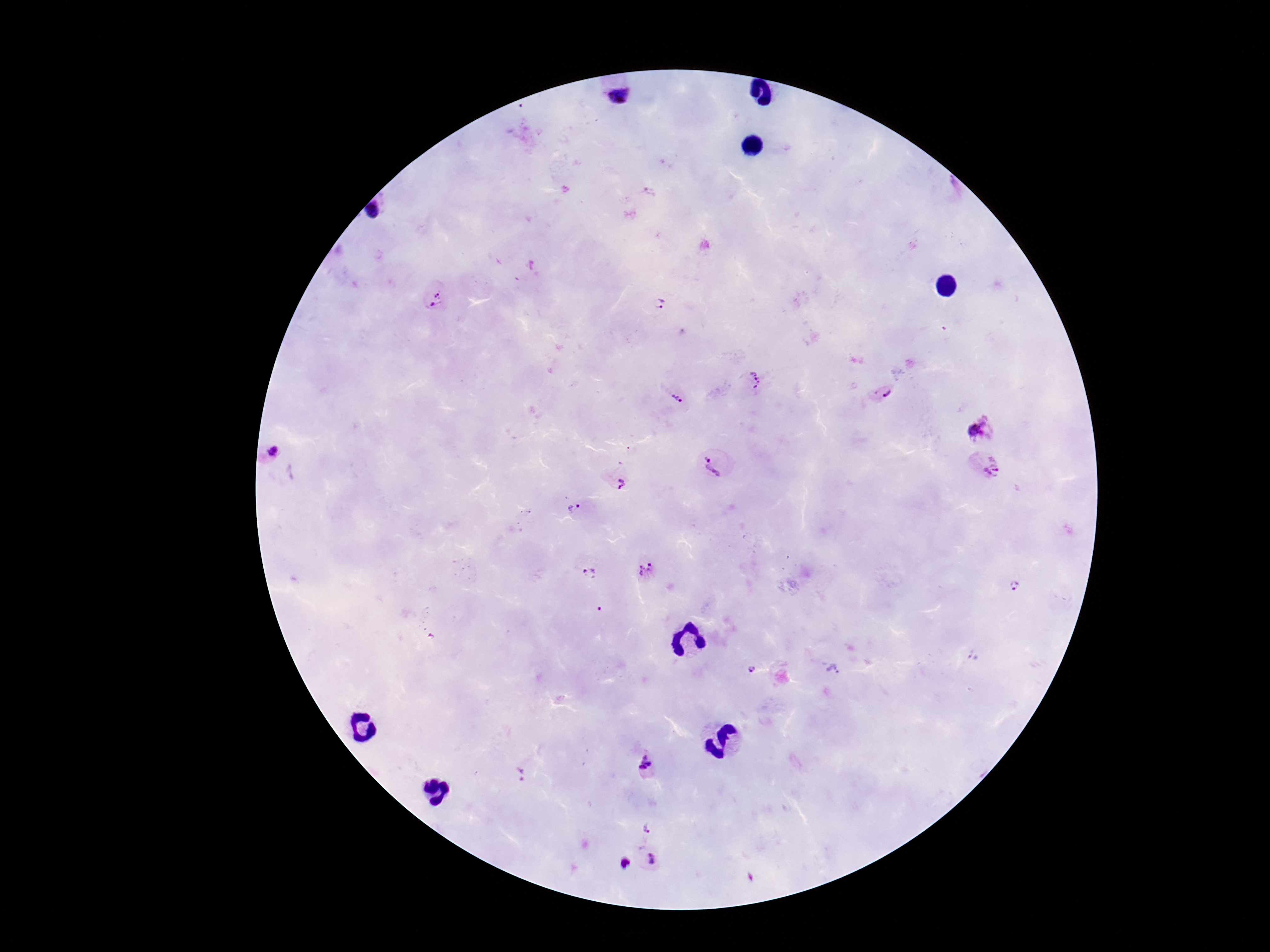

Approximate centers as [x, y] in pixels. Plasmodium parasite locations: [617, 96], [375, 206], [437, 297], [659, 303], [754, 380], [883, 394], [675, 398], [981, 429], [271, 452], [715, 462], [988, 468], [620, 484], [569, 510], [648, 570], [589, 574], [1012, 586], [600, 609], [751, 669], [833, 670], [644, 765], [520, 778], [648, 829], [651, 859], [624, 864]. Photographed through the microscope eyepiece with a smartphone camera. Thick peripheral-blood smear. Giemsa-stained preparation. Image is 1270×952 pixels. Patient malaria status: infected. 100x magnification. Single field of view.